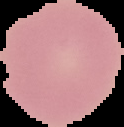

From a thin blood smear. Result: no malaria parasites detected. Image is 124×127 pixels. Segmented cell region on a black background.